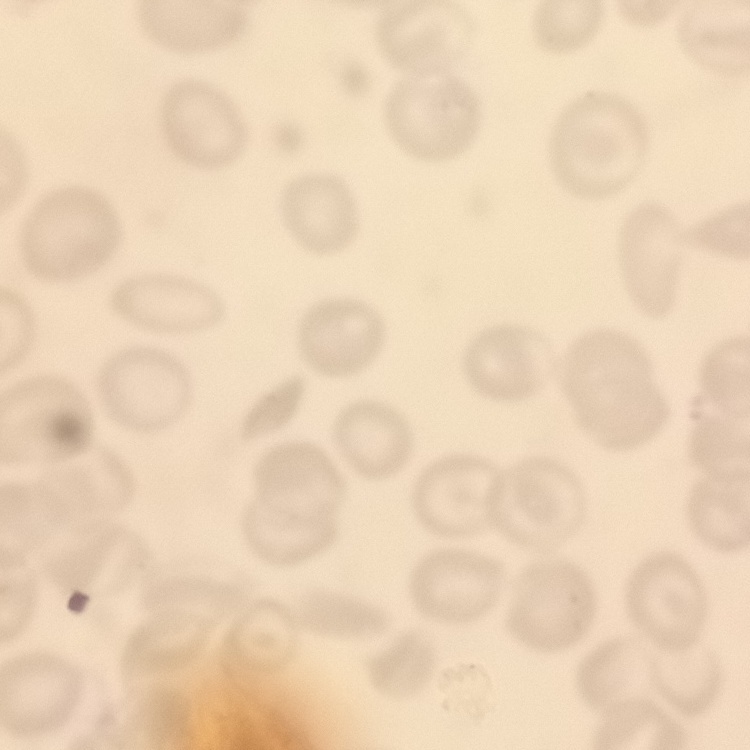

Summary:
  - Erythrocyte morphology: no rouleaux formation
  - Preparation: thin peripheral smear
  - Stain: Field's or Giemsa
  - Image type: square crop of a larger photomicrograph